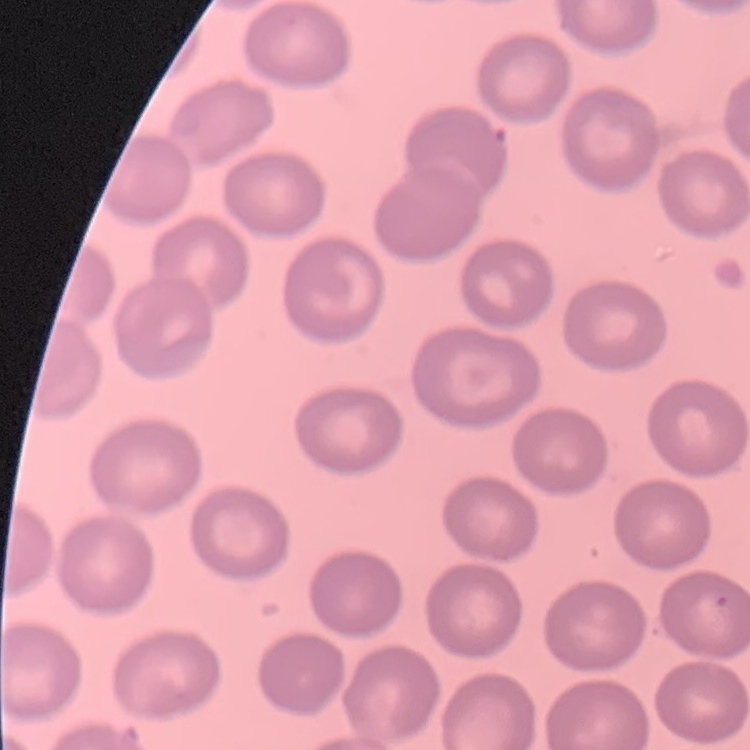 The erythrocytes show no rouleaux formation. Square crop of a larger photomicrograph. Stained with either Field's or Giemsa. Thin peripheral smear.